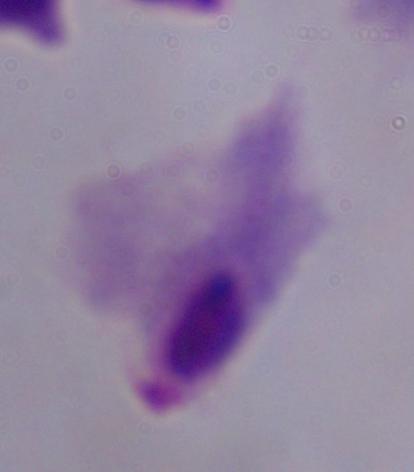
magnification = 1000x
identification = trichomonad
modality = micrograph